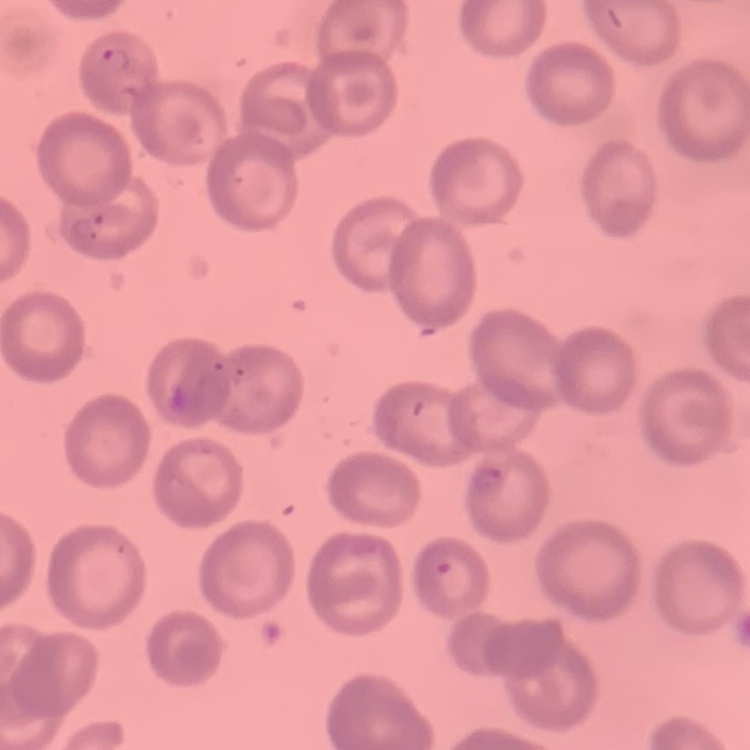
erythrocyte morphology = no rouleaux formation
preparation = thin peripheral smear
stain = Field's or Giemsa
image type = one tile cut from a larger photomicrograph